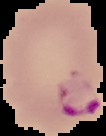
Summary:
  - Malaria status: parasitized
  - Image type: segmented cell region on a black background
  - Image size: 106×136 pixels
  - Preparation: thin blood film